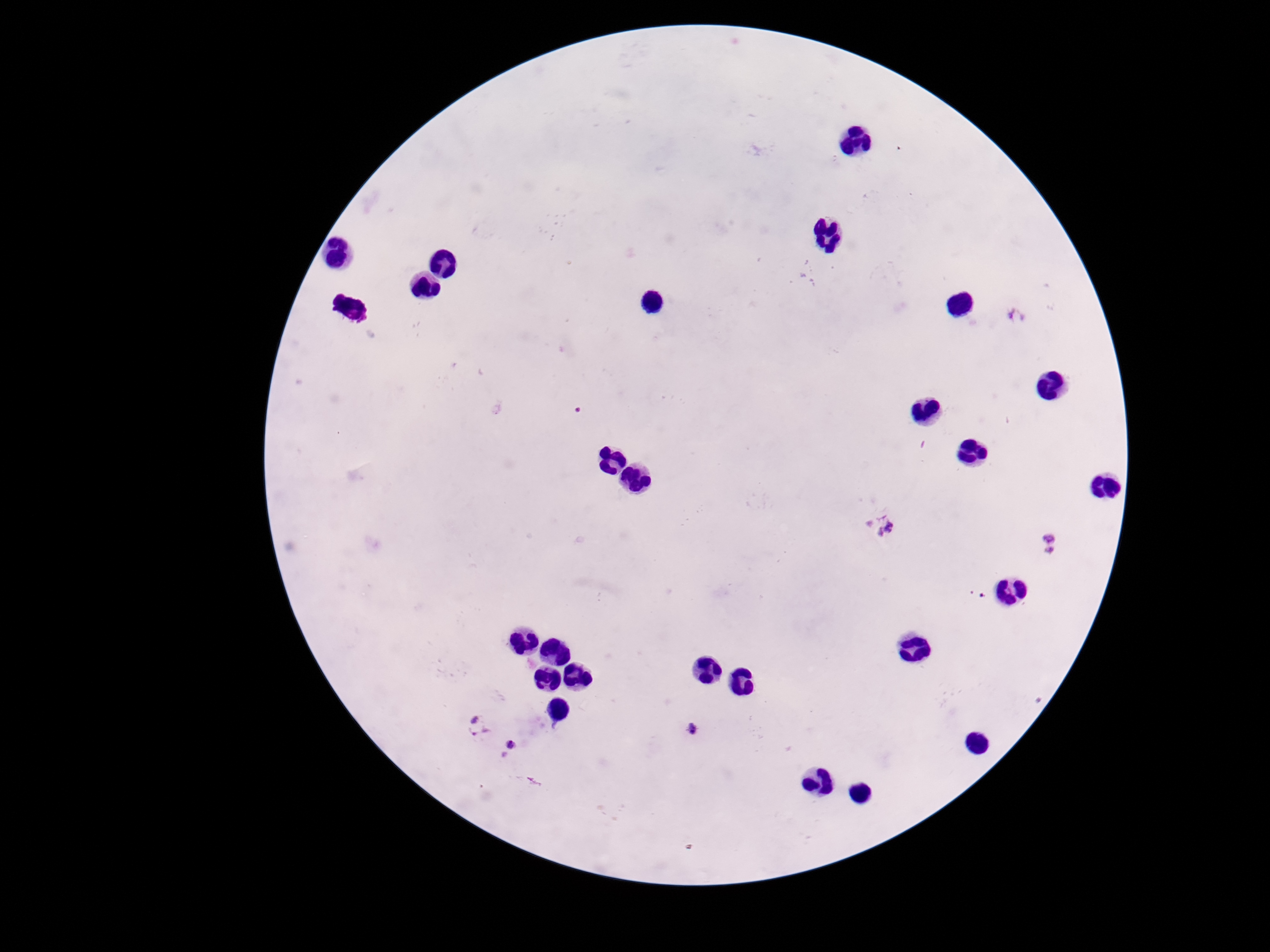
Approximate centers as [x, y] in pixels. Plasmodium parasite locations: [1017, 315], [886, 525], [1048, 543], [478, 723], [690, 729], [513, 752]. 100x magnification. Photographed through the microscope eyepiece with a smartphone camera. Image is 1270×952 pixels. Patient malaria status: positive. Thick blood film. Giemsa stain. Single field of view.